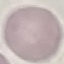

Summary:
  - Result: no malaria parasites seen
  - Capture: smartphone camera at the microscope eyepiece
  - Stain: Giemsa
  - Image type: cell patch, automatically extracted from a larger field of view and resized to 64 × 64 pixels
  - Preparation: thin smear